State the blood parasite species.
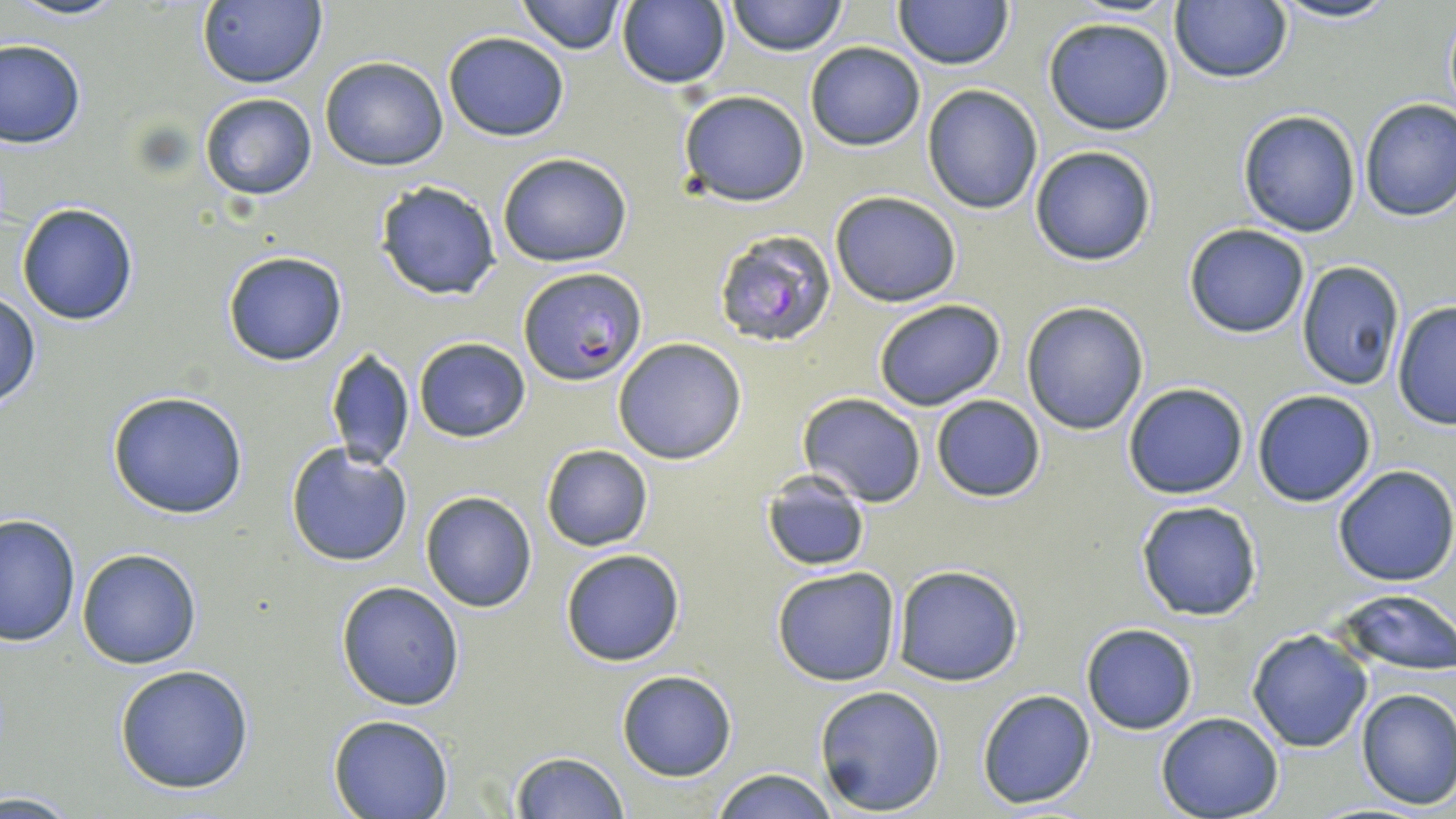
Plasmodium falciparum.

Summary:
  - Coordinate format: approximate bounding boxes as [x1, y1, x2, y2] in pixels
  - Plasmodium falciparum-infected red blood cell locations: [714, 229, 838, 348], [518, 266, 646, 386]
  - Uninfected red blood cell locations: [9, 0, 129, 23], [515, 0, 626, 53], [728, 0, 846, 56], [1170, 0, 1292, 84], [1266, 0, 1405, 24], [195, 1, 326, 88], [894, 1, 1014, 70], [1440, 1, 1455, 127], [615, 2, 731, 88], [1043, 16, 1176, 135], [443, 30, 569, 141], [1, 38, 85, 149], [805, 42, 925, 150], [319, 56, 448, 171], [921, 84, 1043, 213], [678, 91, 810, 206], [199, 93, 318, 201], [1358, 98, 1456, 223], [1238, 108, 1363, 237], [1029, 144, 1158, 266], [497, 152, 632, 268], [374, 180, 501, 300], [828, 191, 962, 308], [16, 202, 139, 325], [1183, 224, 1310, 337], [222, 250, 349, 367], [1297, 261, 1406, 392], [1, 292, 40, 410], [873, 299, 1006, 411], [1021, 301, 1150, 434], [1392, 302, 1456, 429], [412, 336, 530, 442], [613, 338, 747, 464], [324, 346, 414, 471], [1122, 383, 1249, 499], [1252, 388, 1377, 507], [107, 389, 250, 519], [797, 393, 926, 507], [930, 395, 1047, 504], [284, 443, 414, 568], [540, 444, 653, 551], [1332, 465, 1456, 586], [760, 471, 872, 571], [421, 492, 538, 612], [1135, 499, 1264, 621], [1, 513, 80, 646], [77, 547, 202, 667], [559, 548, 686, 667], [771, 565, 902, 686], [892, 565, 1024, 686], [335, 581, 465, 711], [1333, 589, 1456, 674], [1081, 623, 1197, 734], [1247, 629, 1373, 752], [113, 664, 256, 795], [617, 671, 738, 781], [814, 684, 946, 816], [1355, 687, 1456, 810], [975, 688, 1097, 810], [1156, 713, 1284, 819], [327, 714, 454, 819], [509, 751, 628, 818], [708, 767, 840, 819]
  - Modality: optical microscopy
  - Stain: May-Grünwald-Giemsa
  - Magnification: 1000x
  - Field of view: single
  - Preparation: thin blood film
  - Image size: 1456×819 pixels